State which parasite is depicted.
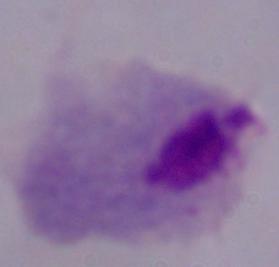
This is a trichomonad.

Micrograph. 1000x magnification.